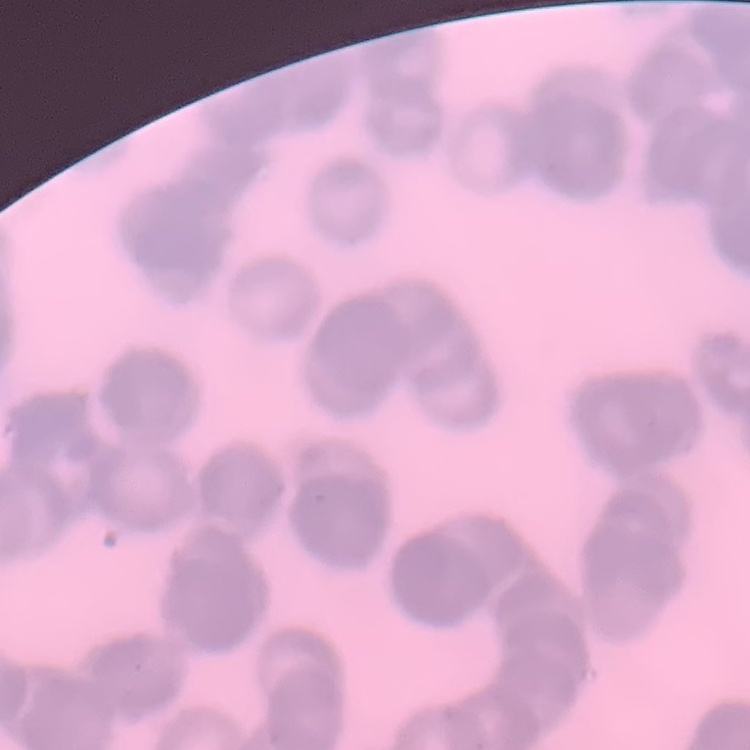

red blood cell morphology = rouleaux formation
preparation = thin blood smear
stain = Field's or Giemsa
image type = square crop of a larger photomicrograph